Locate the P. falciparum-infected red blood cells and any of indeterminate infection status.
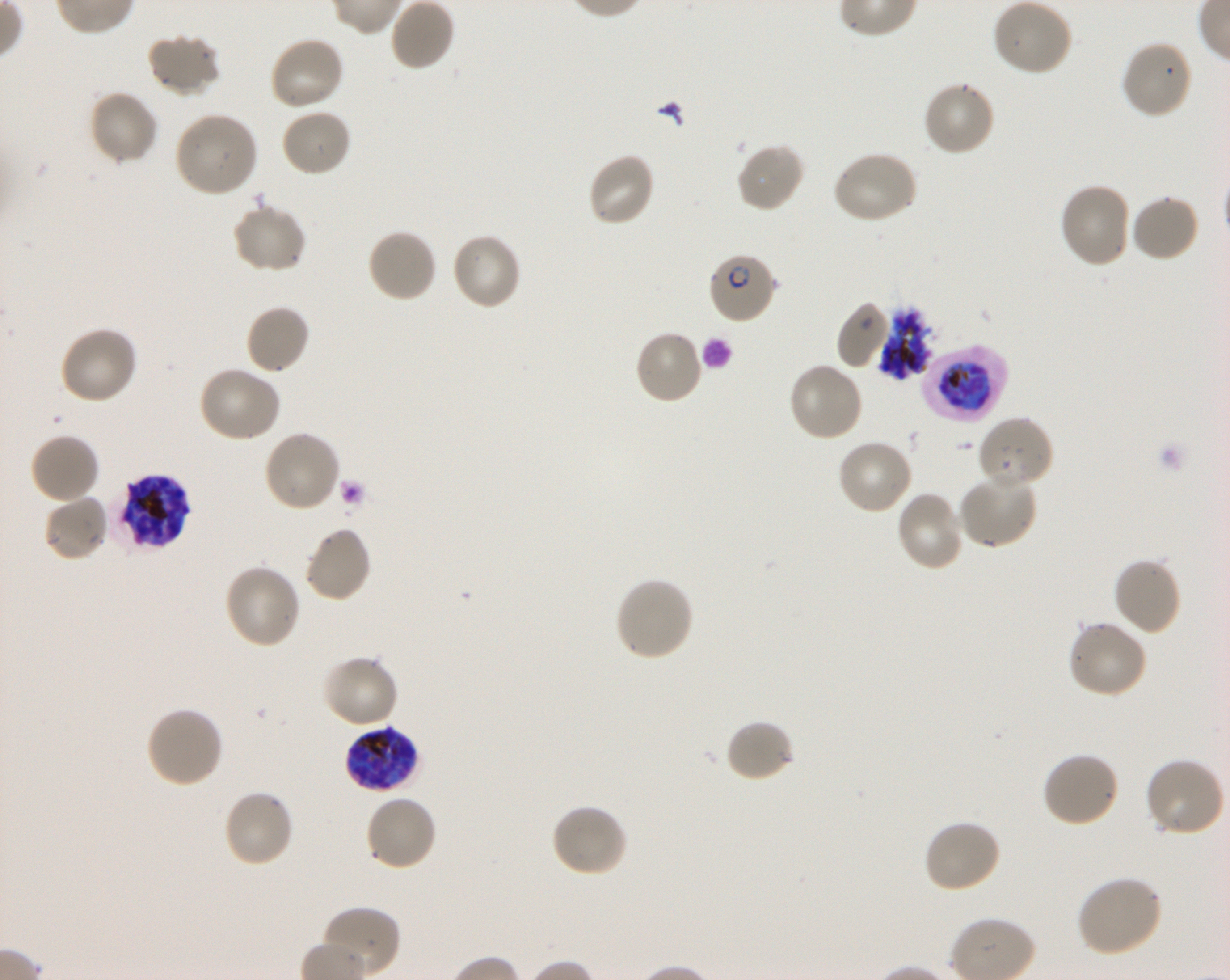
Approximate bounding boxes as [x1, y1, x2, y2] in pixels. Not every red blood cell is marked. A life-cycle stage — or a range of stages, where the recorded stages span more than one — follows each staged infected red blood cell.
Infected red blood cells: [707, 251, 778, 325] early ring to early trophozoite; [922, 346, 1006, 422] early trophozoite to late schizont; [114, 473, 190, 550] schizont; [343, 724, 420, 794] late trophozoite to late schizont.
Red blood cells of indeterminate infection status: [879, 308, 933, 380].

locations of uninfected red blood cells = [992, 0, 1074, 77], [146, 33, 220, 98], [269, 35, 345, 112], [1119, 39, 1194, 120], [921, 79, 996, 157], [88, 90, 159, 166], [281, 107, 353, 177], [173, 110, 260, 198], [736, 141, 807, 214], [832, 151, 918, 226], [586, 152, 656, 228], [1057, 182, 1132, 270], [1129, 194, 1200, 263], [231, 202, 308, 275], [366, 228, 438, 304], [449, 231, 522, 312], [837, 302, 893, 370], [245, 304, 312, 375], [58, 326, 139, 405], [633, 329, 704, 405], [787, 361, 864, 443], [197, 366, 281, 443], [977, 415, 1055, 492], [262, 429, 341, 513], [29, 432, 100, 505], [836, 437, 914, 515], [956, 473, 1038, 549], [895, 490, 965, 572], [42, 494, 110, 563], [303, 525, 373, 604], [1112, 557, 1183, 636], [223, 563, 302, 650], [613, 576, 694, 663], [1067, 620, 1147, 699], [321, 653, 400, 730], [145, 706, 224, 789], [725, 718, 795, 784], [1041, 750, 1121, 828], [1143, 757, 1226, 838], [222, 788, 295, 868], [364, 794, 438, 872], [550, 803, 629, 878], [922, 819, 1002, 894], [1075, 874, 1164, 958], [320, 906, 401, 976]
field of view = one from this slide
stain = Giemsa
objective = 100x, oil immersion, numerical aperture 1.30
preparation = thin blood smear
donor blood group = O+
image size = 1230×980 pixels
culture = in-vitro P. falciparum strain 3D7, shaking